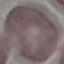

result = no malaria parasites detected
image type = automatically extracted cell patch, resized to 64 × 64 pixels
capture = smartphone through the microscope eyepiece
preparation = thin blood smear
stain = Giemsa